Classify this cell by malaria status.
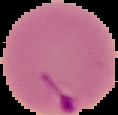
It is parasitized.

preparation = thin blood smear
image size = 118×115 pixels
image type = segmented cell region with the area outside set to black